Report the malaria status of this cell.
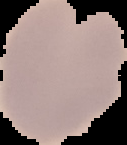

It is uninfected.

Summary:
  - Image type: cell region segmented out of the field of view; surrounding area masked to black
  - Image size: 127×145 pixels
  - Preparation: thin blood film